Name the blood parasite species.
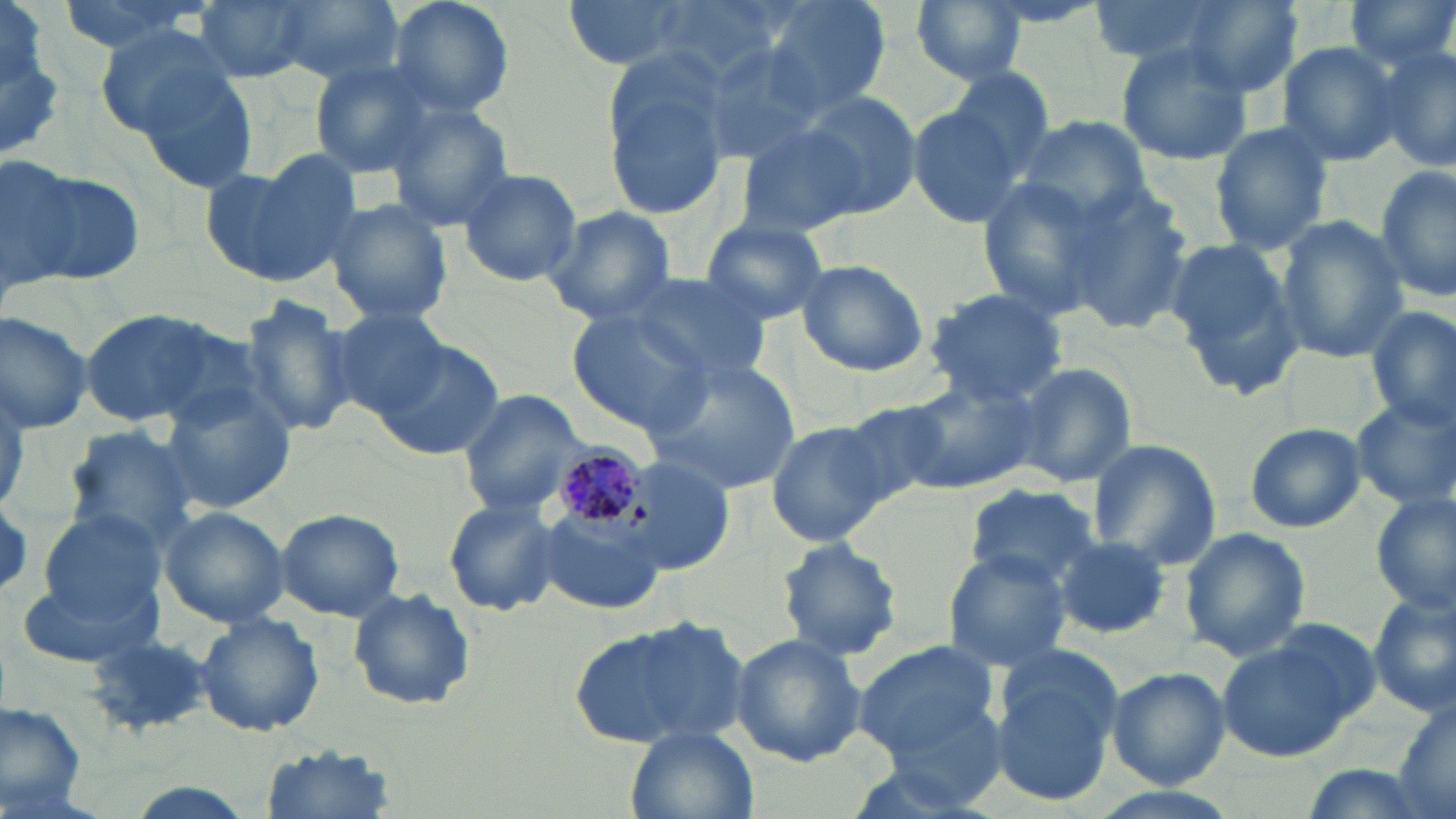

Plasmodium malariae.

Summary:
  - Coordinate format: approximate bounding boxes as (x1,y1)-(x2,y2) corner pairs in pixels
  - Plasmodium malariae-infected red blood cell locations: (548,435)-(645,532)
  - Uninfected red blood cell locations: (51,0)-(213,55), (191,0)-(325,85), (275,0)-(405,81), (386,0)-(515,120), (560,0)-(707,72), (755,0)-(890,117), (1091,0)-(1244,64), (1183,0)-(1304,98), (1344,0)-(1456,69), (912,1)-(1026,85), (97,24)-(243,150), (1371,40)-(1456,168), (695,41)-(830,166), (1114,42)-(1253,168), (1276,42)-(1402,166), (601,52)-(734,222), (309,59)-(440,176), (126,62)-(260,192), (942,65)-(1057,173), (793,89)-(922,220), (908,100)-(1032,228), (388,103)-(515,230), (1012,114)-(1155,231), (1205,120)-(1334,257), (735,123)-(870,241), (202,158)-(356,288), (5,164)-(147,288), (1375,164)-(1456,306), (456,167)-(583,287), (974,175)-(1116,320), (1062,187)-(1194,338), (325,198)-(454,325), (539,205)-(679,325), (1274,215)-(1409,364), (698,219)-(830,325), (1167,237)-(1300,382), (795,258)-(931,378), (616,267)-(774,386), (923,289)-(1069,403), (235,295)-(359,440), (1367,304)-(1456,429), (326,306)-(450,420), (78,308)-(225,426), (0,310)-(94,434), (569,313)-(715,437), (373,339)-(506,461), (646,359)-(799,494), (1008,359)-(1139,490), (897,377)-(1037,495), (158,386)-(298,514), (456,387)-(590,513), (1351,396)-(1456,512), (839,401)-(955,504), (766,419)-(890,548), (1243,421)-(1366,533), (61,427)-(198,552), (1087,439)-(1219,570), (622,455)-(734,576), (964,481)-(1101,592), (1372,492)-(1456,613), (443,494)-(563,617), (158,506)-(291,629), (275,508)-(404,621), (538,511)-(665,617), (41,512)-(166,625), (1179,527)-(1313,662), (774,537)-(904,664), (1052,537)-(1173,639), (941,549)-(1071,670), (16,575)-(160,669), (347,588)-(475,712), (1367,591)-(1456,717), (194,612)-(324,738), (571,614)-(756,753), (1218,626)-(1374,762), (84,629)-(216,736), (729,633)-(865,766), (852,642)-(1002,771), (987,656)-(1122,806), (1106,666)-(1230,789), (1387,699)-(1456,819), (0,702)-(88,813), (626,728)-(756,819), (256,746)-(404,819)
  - Image size: 1456×819 pixels
  - Stain: May-Grünwald-Giemsa
  - Field of view: single
  - Preparation: thin blood smear
  - Modality: optical microscopy
  - Magnification: 1000x